Report the malaria status of this cell.
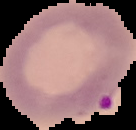
It is parasitized.

{
  "image_type": "segmented cell region with the area outside set to black",
  "image_size": "136×130 pixels",
  "preparation": "thin blood smear"
}